Locate and identify every blood parasite.
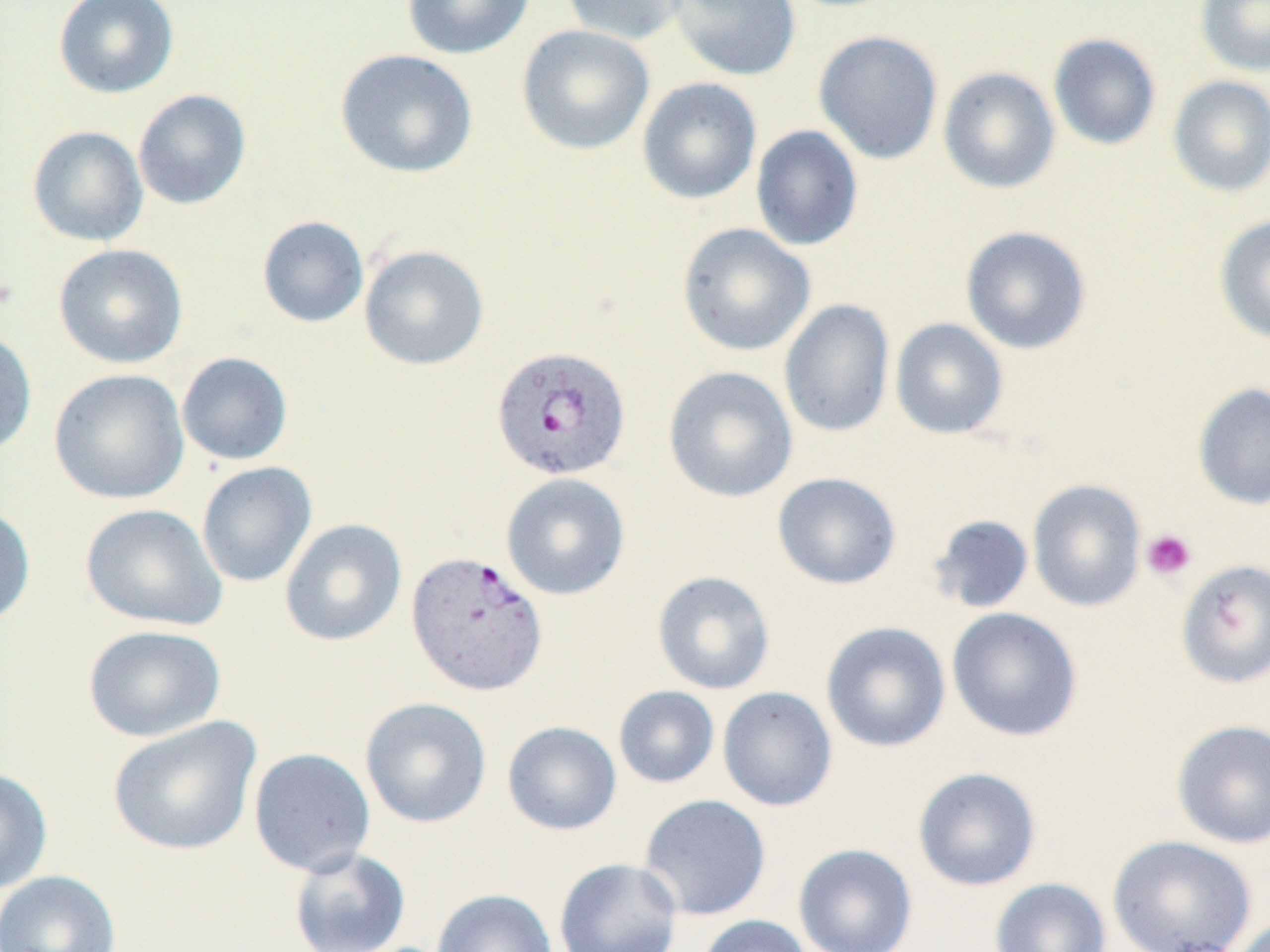
Approximate bounding boxes as [x1, y1, x2, y2] in pixels.
Plasmodium vivax-infected red blood cells: [493, 344, 634, 482], [407, 551, 550, 696].
No Plasmodium falciparum, Plasmodium ovale, Plasmodium malariae, Babesia divergens, or Trypanosoma brucei observed.

Platelet locations: [1141, 529, 1196, 581]. Uninfected red blood cell locations: [53, 0, 179, 99], [403, 0, 534, 59], [560, 0, 690, 45], [667, 0, 800, 81], [1194, 0, 1270, 76], [517, 24, 654, 155], [813, 30, 944, 164], [1048, 33, 1161, 150], [336, 49, 478, 179], [938, 66, 1060, 194], [1167, 75, 1270, 197], [637, 77, 762, 204], [132, 89, 251, 210], [27, 125, 148, 246], [750, 125, 863, 251], [1214, 214, 1270, 345], [257, 216, 369, 328], [677, 223, 816, 356], [960, 225, 1091, 354], [53, 244, 188, 368], [359, 245, 489, 370], [779, 298, 895, 438], [890, 317, 1008, 439], [0, 329, 37, 457], [177, 352, 293, 465], [663, 365, 798, 503], [49, 368, 190, 504], [1192, 381, 1270, 511], [196, 461, 317, 587], [501, 472, 630, 600], [772, 472, 901, 590], [1027, 479, 1147, 612], [0, 503, 36, 627], [80, 504, 227, 631], [928, 514, 1035, 614], [280, 518, 407, 646], [1175, 559, 1270, 689], [652, 570, 775, 694], [946, 607, 1082, 741], [820, 621, 951, 753], [83, 624, 226, 742], [613, 685, 719, 788], [717, 686, 837, 812], [360, 696, 492, 828], [108, 716, 261, 856], [1171, 719, 1270, 848], [502, 720, 622, 835], [248, 747, 376, 876], [0, 766, 53, 894], [913, 766, 1041, 891], [638, 793, 771, 921], [1107, 834, 1257, 952], [793, 843, 918, 952], [289, 846, 411, 952], [554, 858, 682, 952], [0, 870, 121, 952], [991, 877, 1111, 952], [432, 888, 557, 952], [696, 914, 814, 952], [1231, 915, 1270, 952]. Slide-level diagnosis: Plasmodium vivax. Thin blood film. One field of a larger specimen. Image is 1270×952 pixels. May-Grünwald-Giemsa-stained preparation. 1000x magnification. Light microscopy.